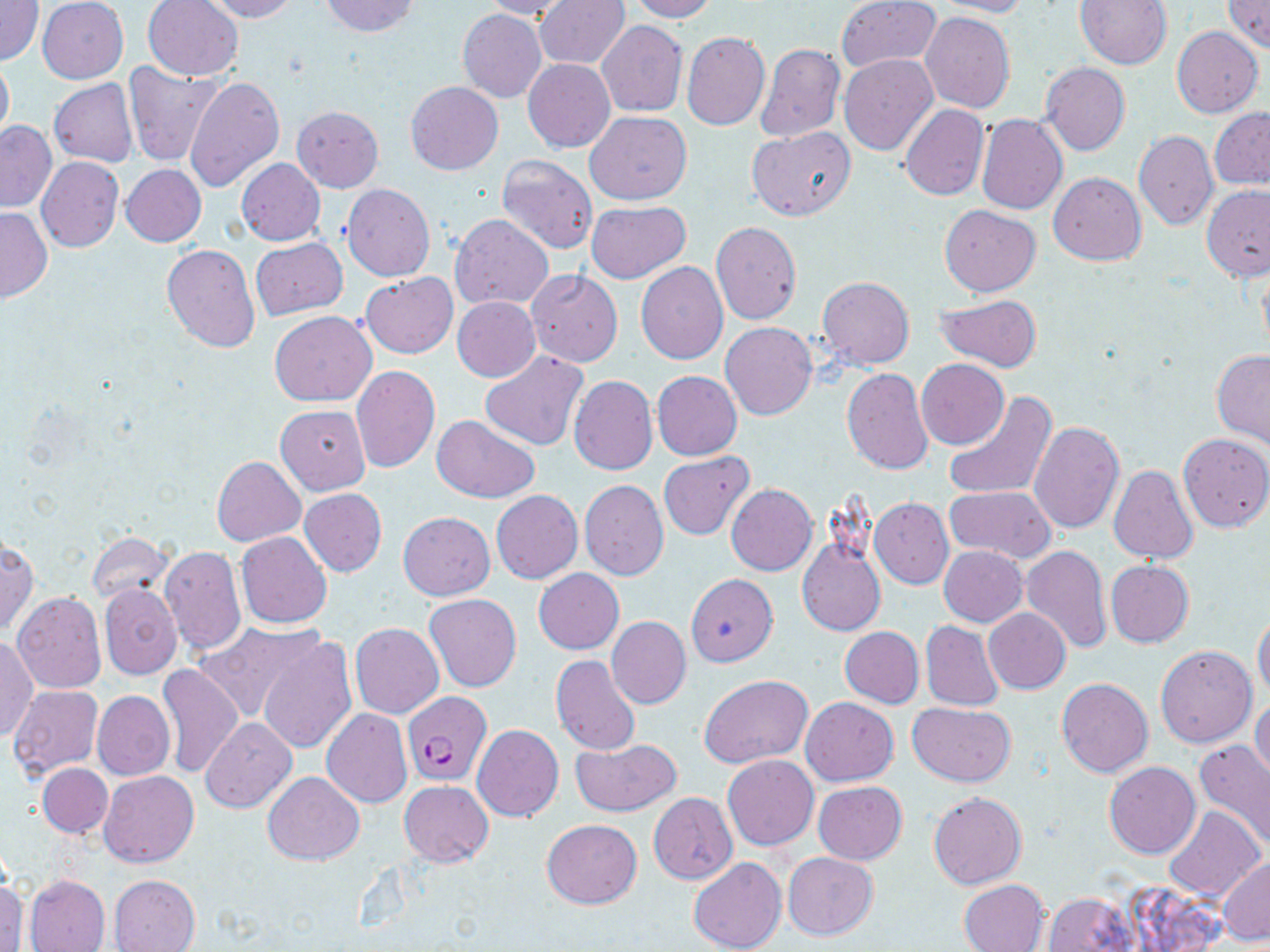
slide-level diagnosis = Plasmodium falciparum
field of view = single
uninfected red blood cell locations = approximate bounding boxes as [x1, y1, x2, y2] in pixels: [37, 0, 128, 84], [199, 0, 299, 22], [317, 0, 420, 38], [481, 0, 574, 20], [536, 0, 628, 69], [626, 0, 717, 22], [835, 0, 942, 74], [929, 0, 1033, 17], [1076, 0, 1172, 68], [1224, 0, 1270, 51], [1, 1, 43, 66], [142, 1, 244, 80], [456, 9, 547, 102], [920, 12, 1015, 113], [597, 20, 687, 117], [1172, 25, 1263, 117], [682, 32, 770, 131], [756, 43, 845, 143], [0, 54, 14, 145], [838, 54, 938, 156], [523, 59, 616, 153], [124, 61, 223, 167], [1040, 63, 1130, 154], [185, 75, 284, 192], [49, 79, 138, 167], [406, 81, 503, 175], [898, 103, 990, 201], [292, 106, 382, 192], [1209, 107, 1270, 189], [585, 111, 692, 204], [976, 113, 1068, 214], [1, 120, 56, 212], [747, 126, 857, 219], [1134, 130, 1218, 230], [497, 154, 598, 254], [36, 156, 123, 252], [236, 158, 325, 245], [121, 164, 206, 247], [1049, 172, 1146, 265], [341, 183, 434, 281], [1202, 185, 1270, 279], [586, 200, 691, 283], [939, 204, 1040, 295], [0, 207, 52, 304], [450, 213, 554, 311], [710, 222, 802, 325], [251, 239, 347, 320], [161, 244, 261, 352], [1256, 255, 1270, 363], [636, 262, 727, 364], [527, 270, 623, 368], [360, 273, 457, 358], [817, 275, 914, 369], [935, 293, 1043, 373], [452, 297, 540, 381], [269, 311, 377, 407], [721, 322, 818, 420], [479, 350, 590, 453], [1212, 350, 1270, 448], [917, 360, 1009, 448], [351, 365, 440, 473], [841, 367, 932, 474], [651, 370, 743, 461], [569, 376, 658, 475], [944, 391, 1057, 499], [276, 405, 370, 495], [432, 414, 540, 501], [1028, 421, 1125, 534], [1179, 432, 1270, 531], [658, 452, 753, 539], [211, 455, 305, 547], [1108, 464, 1198, 563], [579, 479, 668, 580], [727, 484, 817, 575], [945, 486, 1055, 563], [299, 488, 387, 576], [490, 490, 583, 583], [870, 497, 953, 589], [399, 511, 495, 599], [236, 531, 332, 628], [90, 535, 174, 604], [0, 537, 38, 636], [797, 538, 886, 637], [1020, 545, 1112, 653], [159, 546, 245, 655], [940, 546, 1027, 626], [1105, 560, 1194, 648], [533, 568, 624, 654], [686, 574, 778, 666], [99, 582, 181, 679], [12, 592, 106, 693], [423, 592, 522, 692], [984, 608, 1071, 694], [1253, 610, 1270, 698], [606, 616, 691, 709], [920, 621, 1004, 711], [197, 622, 324, 722], [351, 623, 443, 718], [839, 627, 924, 707], [0, 636, 38, 744], [258, 637, 358, 754], [1156, 645, 1256, 748], [551, 655, 640, 755], [156, 662, 244, 778], [699, 674, 812, 767], [1056, 677, 1153, 777], [9, 686, 104, 777], [92, 691, 174, 779], [800, 697, 899, 786], [1250, 697, 1270, 782], [907, 701, 1016, 785], [322, 709, 412, 808], [201, 718, 297, 814], [472, 724, 564, 821], [570, 737, 682, 815], [1195, 740, 1270, 850], [722, 754, 818, 850], [1104, 762, 1199, 858], [37, 763, 113, 838], [99, 770, 199, 867], [263, 771, 364, 865], [399, 781, 492, 866], [814, 781, 907, 863], [928, 791, 1027, 889], [649, 793, 737, 883], [1163, 806, 1266, 901], [541, 819, 642, 909], [782, 851, 878, 941], [1217, 857, 1270, 945], [688, 858, 786, 952], [109, 874, 200, 951], [24, 875, 110, 951], [0, 877, 26, 952], [959, 879, 1049, 952], [1043, 892, 1138, 951]
stain = May-Grünwald-Giemsa
magnification = 1000x
Plasmodium falciparum-infected red blood cell locations = approximate bounding boxes as [x1, y1, x2, y2] in pixels: [402, 691, 490, 785]
preparation = thin blood film
image size = 1270×952 pixels
modality = light microscopy